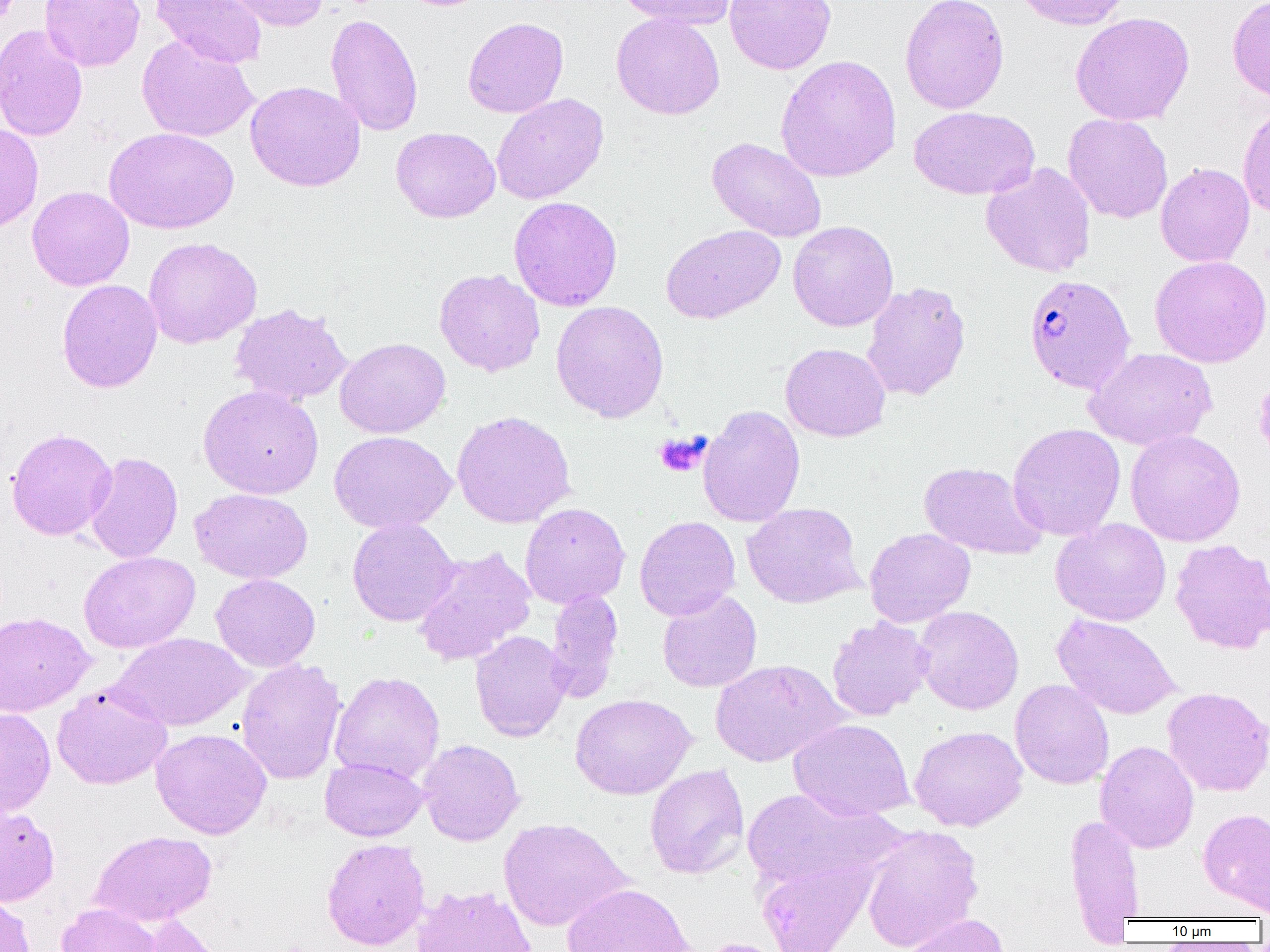

Summary:
  - Coordinate format: approximate bounding boxes as named x1/y1/x2/y2 corners in pixels
  - Platelet locations: (x1=653, y1=432, x2=709, y2=478)
  - Plasmodium falciparum-infected red blood cell locations: (x1=1023, y1=274, x2=1136, y2=394)
  - Uninfected red blood cell locations: (x1=40, y1=0, x2=145, y2=72), (x1=150, y1=0, x2=267, y2=69), (x1=216, y1=0, x2=330, y2=32), (x1=617, y1=0, x2=736, y2=30), (x1=724, y1=0, x2=837, y2=74), (x1=900, y1=0, x2=1010, y2=115), (x1=1013, y1=0, x2=1133, y2=30), (x1=1227, y1=0, x2=1270, y2=103), (x1=1070, y1=12, x2=1194, y2=126), (x1=325, y1=13, x2=423, y2=137), (x1=611, y1=13, x2=725, y2=120), (x1=463, y1=17, x2=569, y2=118), (x1=0, y1=24, x2=88, y2=142), (x1=136, y1=35, x2=258, y2=142), (x1=776, y1=55, x2=901, y2=182), (x1=245, y1=81, x2=365, y2=192), (x1=490, y1=93, x2=609, y2=204), (x1=1237, y1=103, x2=1270, y2=218), (x1=909, y1=106, x2=1039, y2=200), (x1=1063, y1=113, x2=1173, y2=223), (x1=0, y1=123, x2=44, y2=234), (x1=391, y1=126, x2=500, y2=223), (x1=104, y1=127, x2=239, y2=234), (x1=706, y1=136, x2=827, y2=242), (x1=981, y1=162, x2=1096, y2=277), (x1=1155, y1=162, x2=1255, y2=267), (x1=26, y1=185, x2=134, y2=291), (x1=509, y1=196, x2=622, y2=311), (x1=788, y1=220, x2=899, y2=332), (x1=661, y1=224, x2=785, y2=323), (x1=143, y1=237, x2=262, y2=349), (x1=1149, y1=255, x2=1270, y2=368), (x1=434, y1=268, x2=545, y2=376), (x1=56, y1=279, x2=162, y2=393), (x1=861, y1=281, x2=971, y2=401), (x1=551, y1=300, x2=669, y2=422), (x1=229, y1=303, x2=353, y2=405), (x1=335, y1=337, x2=451, y2=438), (x1=781, y1=343, x2=890, y2=442), (x1=1084, y1=348, x2=1217, y2=450), (x1=197, y1=385, x2=324, y2=499), (x1=698, y1=404, x2=806, y2=527), (x1=451, y1=410, x2=576, y2=528), (x1=1007, y1=422, x2=1126, y2=541), (x1=6, y1=428, x2=117, y2=541), (x1=1125, y1=429, x2=1245, y2=547), (x1=329, y1=431, x2=456, y2=533), (x1=84, y1=451, x2=183, y2=563), (x1=918, y1=461, x2=1047, y2=559), (x1=190, y1=488, x2=313, y2=584), (x1=520, y1=502, x2=630, y2=608), (x1=742, y1=502, x2=864, y2=608), (x1=634, y1=516, x2=740, y2=621), (x1=347, y1=517, x2=459, y2=626), (x1=1051, y1=517, x2=1171, y2=625), (x1=864, y1=527, x2=975, y2=627), (x1=1169, y1=538, x2=1270, y2=654), (x1=411, y1=546, x2=536, y2=666), (x1=78, y1=551, x2=200, y2=653), (x1=211, y1=573, x2=321, y2=672), (x1=545, y1=590, x2=623, y2=702), (x1=657, y1=590, x2=762, y2=693), (x1=913, y1=605, x2=1024, y2=715), (x1=0, y1=611, x2=95, y2=716), (x1=1052, y1=613, x2=1180, y2=720), (x1=826, y1=615, x2=934, y2=721), (x1=469, y1=630, x2=572, y2=742), (x1=110, y1=632, x2=252, y2=731), (x1=709, y1=658, x2=847, y2=767), (x1=235, y1=659, x2=346, y2=785), (x1=329, y1=671, x2=445, y2=783), (x1=1010, y1=679, x2=1114, y2=789), (x1=52, y1=684, x2=173, y2=790), (x1=1162, y1=686, x2=1270, y2=797), (x1=570, y1=694, x2=696, y2=799), (x1=0, y1=708, x2=56, y2=816), (x1=788, y1=719, x2=915, y2=821), (x1=909, y1=725, x2=1028, y2=831), (x1=150, y1=728, x2=271, y2=839), (x1=417, y1=739, x2=525, y2=846), (x1=1095, y1=740, x2=1199, y2=853), (x1=320, y1=757, x2=427, y2=841), (x1=644, y1=763, x2=749, y2=879), (x1=742, y1=787, x2=901, y2=891), (x1=0, y1=800, x2=60, y2=906), (x1=1198, y1=807, x2=1270, y2=913), (x1=1064, y1=814, x2=1145, y2=932), (x1=498, y1=817, x2=633, y2=931), (x1=861, y1=825, x2=982, y2=951), (x1=90, y1=830, x2=217, y2=926), (x1=321, y1=838, x2=430, y2=950), (x1=756, y1=856, x2=876, y2=952), (x1=562, y1=882, x2=695, y2=952), (x1=411, y1=885, x2=537, y2=952), (x1=0, y1=894, x2=36, y2=952), (x1=56, y1=903, x2=161, y2=952), (x1=902, y1=913, x2=1009, y2=952), (x1=133, y1=914, x2=226, y2=952), (x1=694, y1=937, x2=788, y2=952)
  - Slide-level diagnosis: Plasmodium falciparum
  - Preparation: thin blood film
  - Image size: 1270×952 pixels
  - Modality: light microscopy
  - Field of view: one of a larger specimen
  - Magnification: 1000x